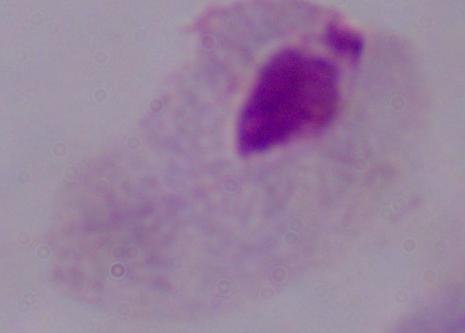

magnification = 1000x
identification = trichomonad
modality = micrograph